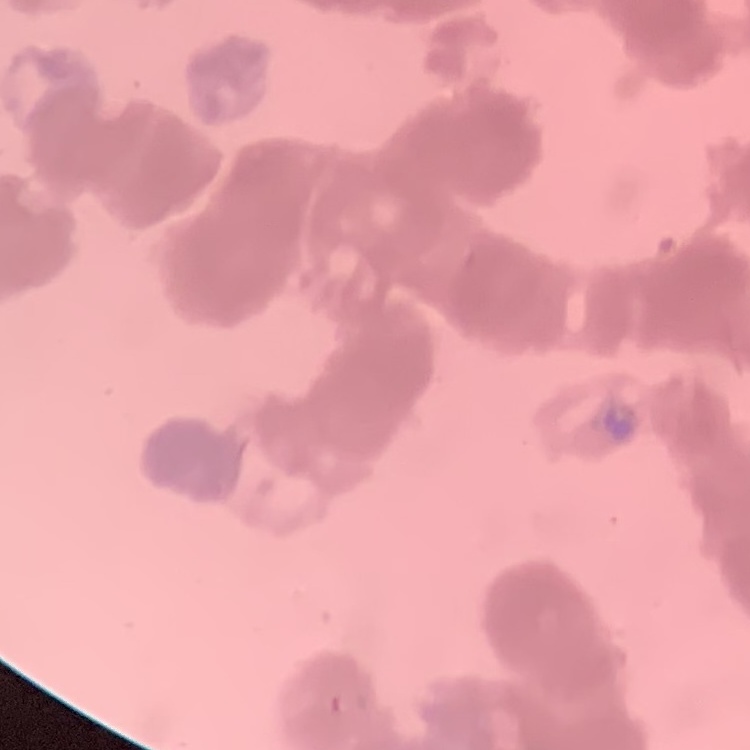 The erythrocytes exhibit rouleaux formation. Thin blood film. Field's or Giemsa stain. One tile cut from a larger photomicrograph.